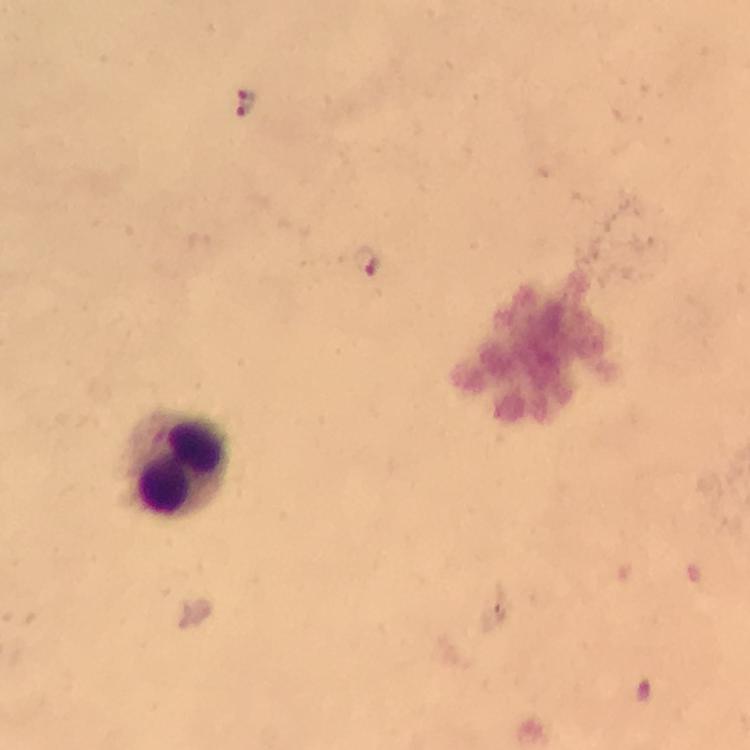
capture = smartphone mounted on the microscope
magnification = 100x
context = from a diagnostic examination for malaria
stain = Giemsa
cropped from = a single field of view
preparation = thick blood film
image size = 750×750 pixels
leukocyte locations = approximate object centers, in pixels from the top-left corner: (x=177, y=464)
Plasmodium parasite locations = approximate object centers, in pixels from the top-left corner: (x=245, y=104), (x=365, y=262)
immersion oil = applied